Comment on the morphology of the erythrocytes.
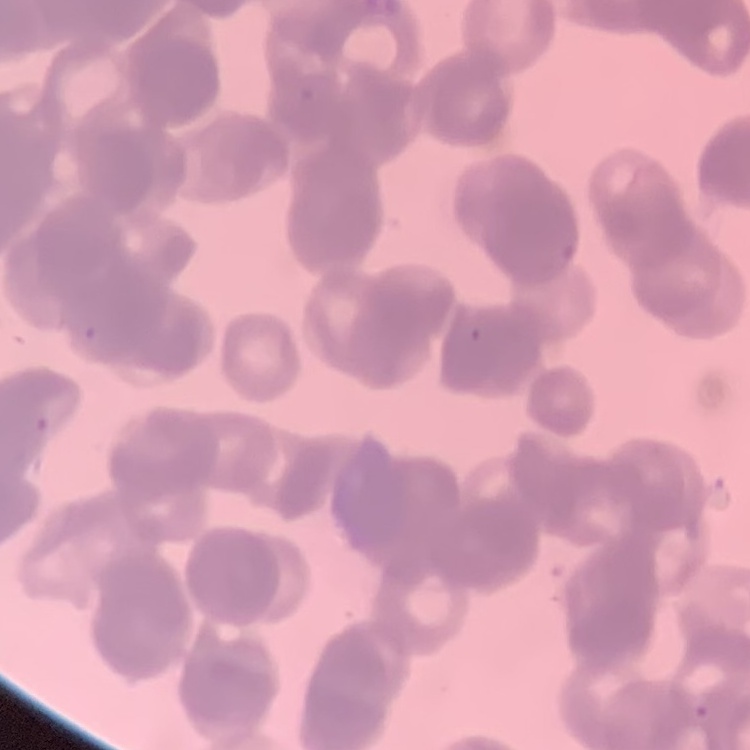
They show rouleaux formation.

Stained with either Field's or Giemsa. Thin peripheral smear. Square crop of a larger photomicrograph.